Assess this cell for malaria.
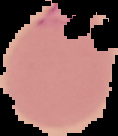
Parasitized.

preparation = thin blood smear
image size = 118×136 pixels
image type = segmented cell region on a black background